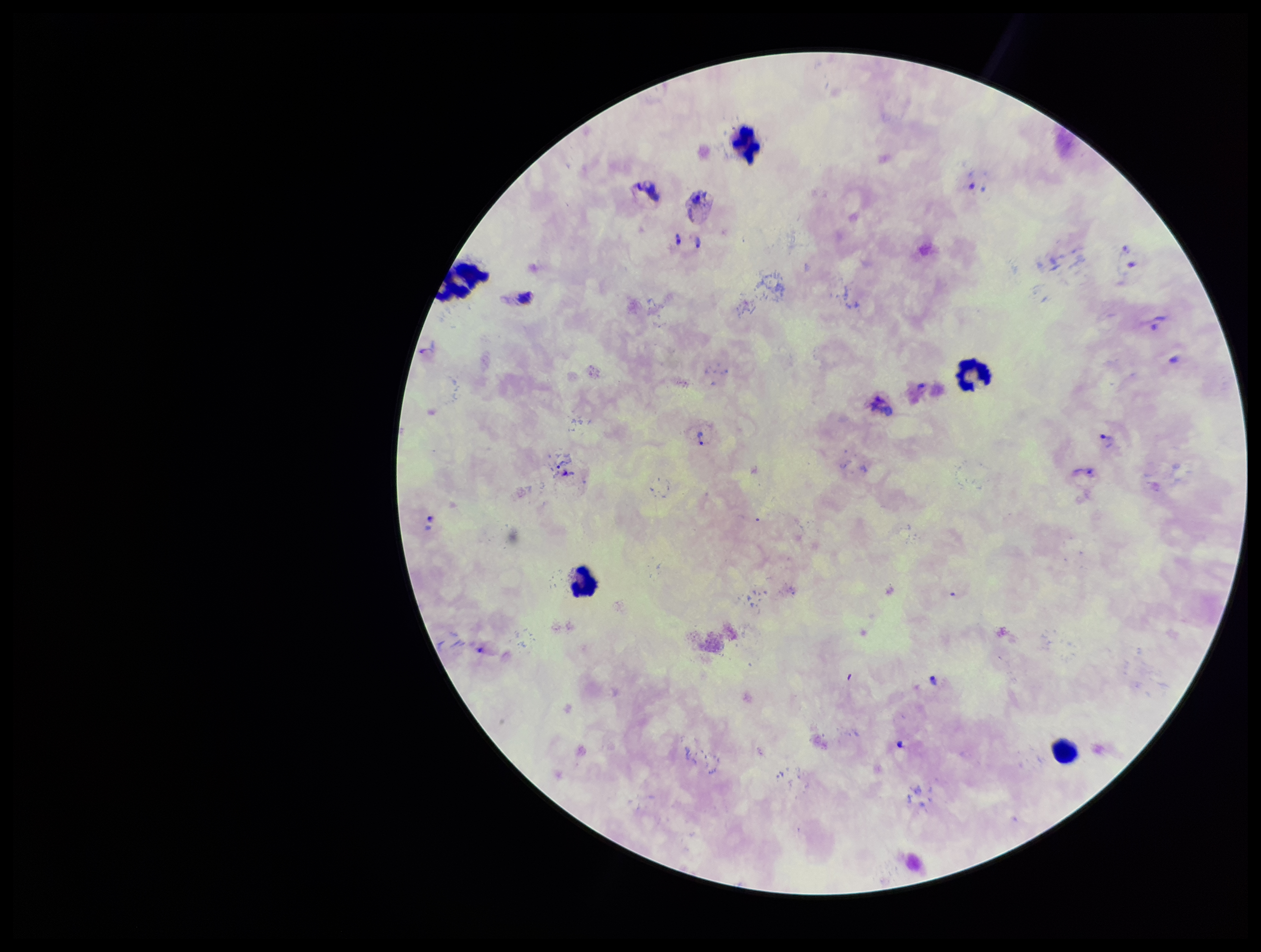
{
  "leukocyte_count": 5,
  "field_of_view": "single",
  "parasite_count": 10,
  "species_reported_for_this_patient": "Plasmodium vivax",
  "preparation": "thick smear",
  "stain": "Giemsa",
  "patient_malaria_status": "infected",
  "plasmodium_parasites": "detected",
  "image_size": "1261×952 pixels",
  "capture": "smartphone photograph through the microscope eyepiece"
}